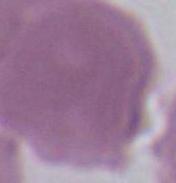
Summary:
  - Modality: photomicrograph
  - Identification: erythrocyte
  - Magnification: 1000x